Comment on the morphology of the red blood cells.
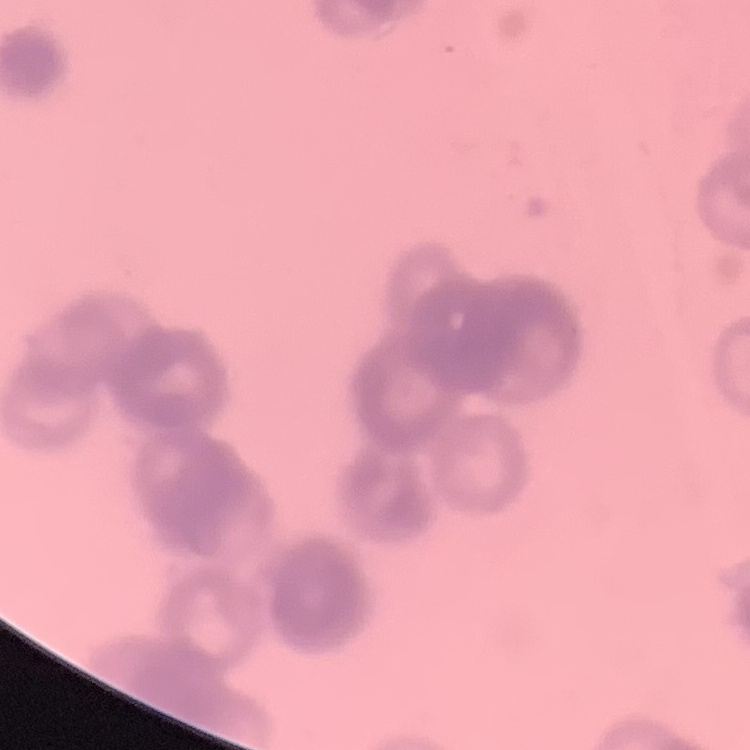
Rouleaux formation.

Stained with either Field's or Giemsa. Thin peripheral smear. Square crop of a larger photomicrograph.